Report the malaria status of this cell.
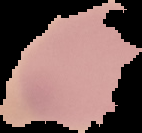

Uninfected.

Segmented cell region on a black background. From a thin blood smear. Image is 142×133 pixels.